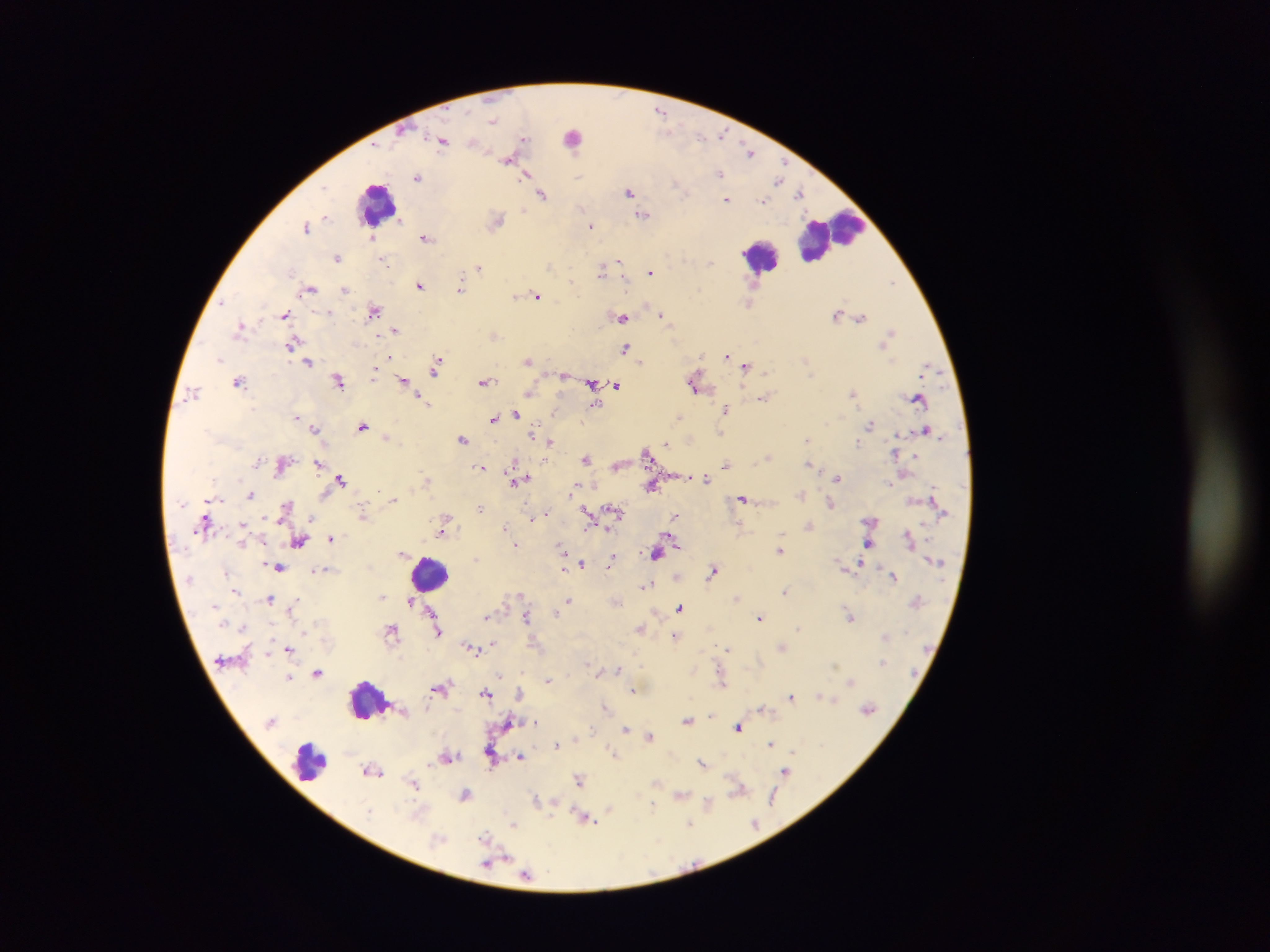

preparation = thick blood film
capture = mobile-phone photograph through a microscope
malaria parasite locations = approximate centers as {x, y} in pixels: {660, 111}, {492, 120}, {722, 134}, {572, 135}, {524, 138}, {700, 138}, {442, 141}, {750, 151}, {507, 159}, {719, 173}, {781, 174}, {527, 175}, {418, 177}, {578, 177}, {778, 180}, {676, 184}, {629, 191}, {800, 193}, {542, 194}, {727, 199}, {763, 201}, {644, 215}, {327, 216}, {400, 219}, {497, 220}, {307, 226}, {591, 226}, {372, 238}, {426, 238}, {337, 257}, {385, 262}, {618, 262}, {711, 263}, {479, 268}, {602, 271}, {650, 272}, {571, 280}, {892, 282}, {420, 285}, {460, 287}, {310, 290}, {345, 290}, {515, 296}, {537, 296}, {221, 303}, {748, 304}, {374, 311}, {839, 313}, {329, 314}, {662, 314}, {285, 315}, {622, 317}, {861, 317}, {239, 328}, {396, 331}, {890, 332}, {290, 344}, {626, 347}, {727, 355}, {219, 358}, {528, 360}, {641, 361}, {308, 362}, {437, 366}, {745, 367}, {375, 370}, {765, 372}, {564, 375}, {403, 379}, {339, 380}, {238, 381}, {485, 382}, {694, 383}, {592, 385}, {616, 385}, {193, 392}, {528, 392}, {854, 393}, {763, 398}, {918, 398}, {421, 399}, {594, 405}, {725, 409}, {516, 413}, {297, 417}, {680, 417}, {493, 418}, {871, 423}, {363, 426}, {315, 428}, {721, 433}, {533, 435}, {462, 439}, {807, 439}, {549, 442}, {666, 443}, {857, 443}, {647, 452}, {916, 456}, {768, 457}, {586, 458}, {317, 463}, {809, 463}, {726, 464}, {480, 467}, {706, 477}, {838, 478}, {341, 479}, {518, 479}, {427, 480}, {891, 484}, {652, 487}, {574, 489}, {801, 494}, {251, 495}, {393, 499}, {742, 499}, {831, 504}, {479, 507}, {617, 512}, {545, 513}, {363, 515}, {589, 515}, {675, 516}, {532, 518}, {444, 523}, {243, 524}, {505, 526}, {331, 538}, {299, 542}, {869, 543}, {515, 546}, {779, 551}, {563, 552}, {400, 553}, {655, 553}, {475, 559}, {611, 560}, {581, 564}, {860, 565}, {279, 568}, {564, 568}, {320, 570}, {713, 571}, {226, 572}, {677, 575}, {894, 576}, {646, 585}, {237, 591}, {785, 591}, {521, 595}, {382, 596}, {737, 597}, {269, 599}, {569, 599}, {410, 603}, {680, 608}, {432, 610}, {555, 614}, {487, 616}, {849, 616}, {526, 617}, {760, 618}, {243, 627}, {639, 628}, {798, 629}, {392, 630}, {438, 632}, {675, 635}, {885, 637}, {493, 644}, {782, 647}, {290, 648}, {472, 648}, {727, 648}, {268, 652}, {883, 662}, {587, 663}, {835, 664}, {618, 669}, {318, 672}, {500, 675}, {289, 677}, {548, 681}, {722, 681}, {850, 682}, {440, 687}, {633, 691}, {486, 693}, {520, 693}, {821, 694}, {791, 696}, {833, 699}, {605, 707}, {761, 709}, {868, 710}, {711, 716}, {687, 719}, {508, 723}, {536, 723}, {738, 727}, {625, 729}, {592, 730}, {649, 736}, {770, 744}, {556, 745}, {794, 751}, {614, 754}, {449, 757}, {521, 757}, {491, 761}, {702, 762}, {429, 764}, {372, 771}, {785, 772}, {579, 779}, {655, 782}, {413, 784}, {738, 790}, {466, 794}, {680, 794}, {773, 799}, {537, 800}, {707, 802}, {652, 806}, {610, 808}, {370, 812}, {585, 819}, {754, 823}, {690, 824}, {513, 825}, {485, 835}, {490, 862}, {527, 875}
country = Ghana
leukocyte locations = approximate centers as {x, y} in pixels: {375, 201}, {829, 236}, {760, 254}, {431, 573}, {368, 701}, {309, 762}
field of view = single
image size = 1270×952 pixels